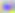

Summary:
  - Magnification: 400x
  - Modality: photomicrograph
  - Identification: Toxoplasma gondii